Report the malaria status of this cell.
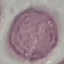
Uninfected.

preparation = thin blood film
capture = smartphone camera at the microscope eyepiece
image type = cell patch, automatically extracted from a larger field of view and resized to 64 × 64 pixels
stain = Giemsa